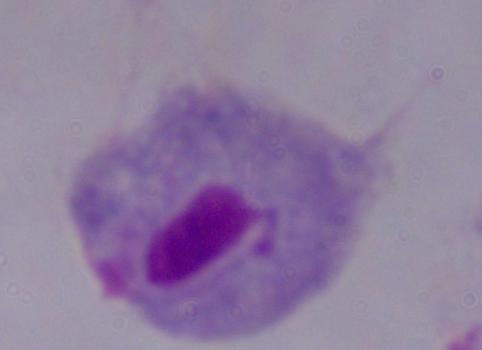

Summary:
  - Identification: trichomonad
  - Magnification: 1000x
  - Modality: micrograph